Comment on the morphology of the erythrocytes.
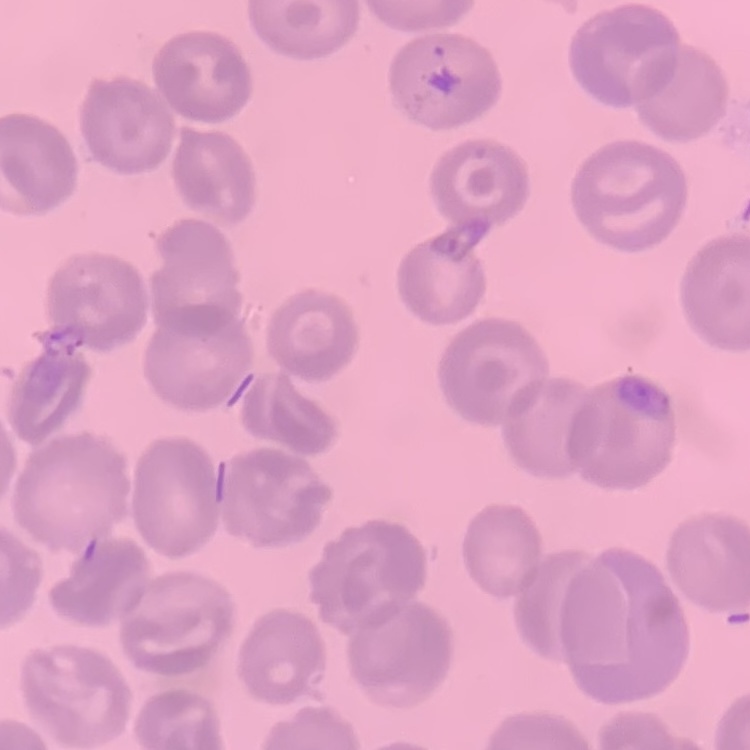

They show no rouleaux formation.

Square crop of a larger photomicrograph. Thin peripheral smear. Field's or Giemsa stain.